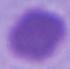
Micrograph. 1000x magnification. A red blood cell is shown.